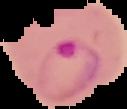
Malaria status: parasitized. Cell region segmented out of the field of view; the surrounding area is masked to black. From a thin blood film. Image is 127×109 pixels.